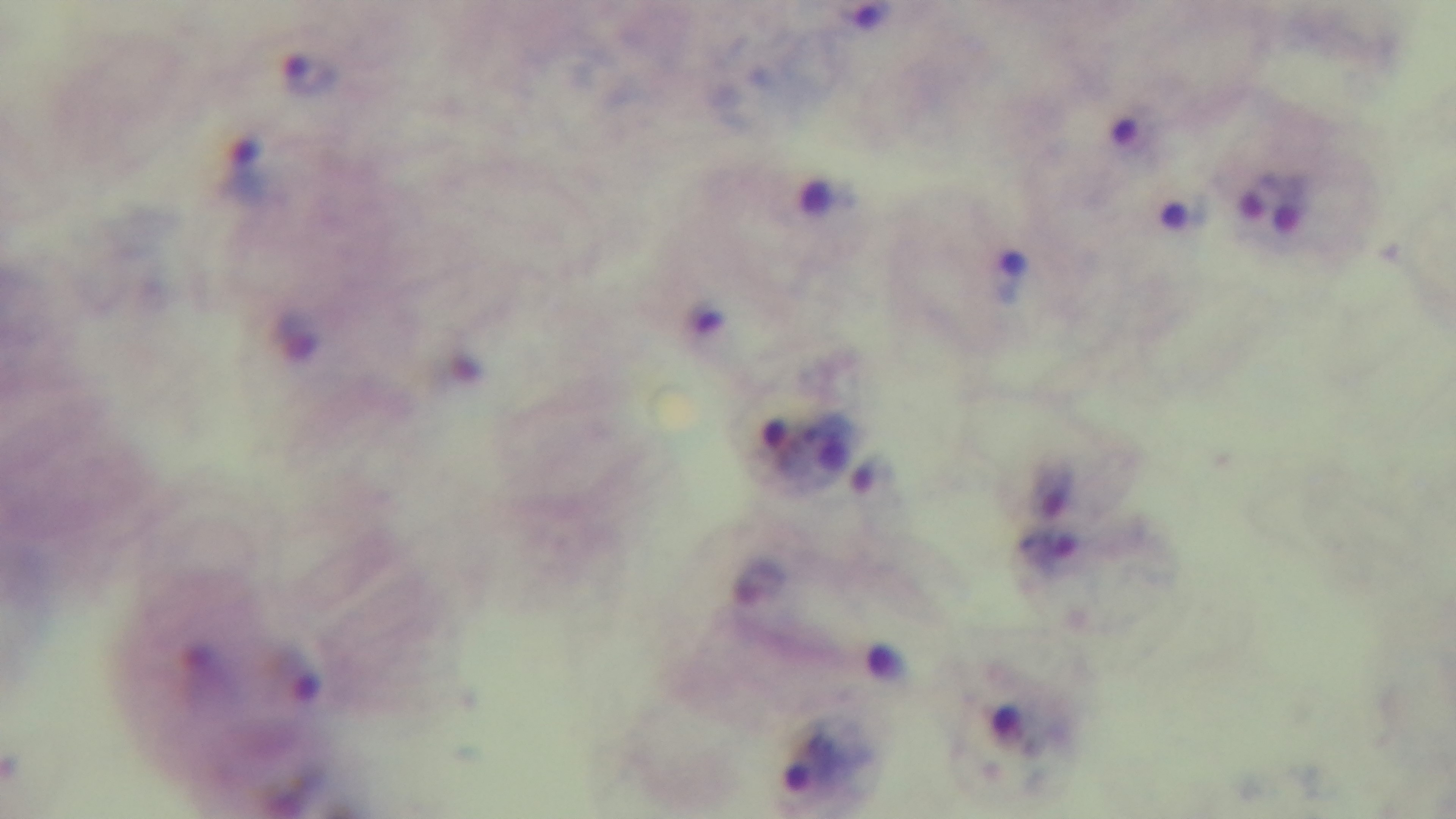

Summary:
  - Preparation: thick
  - Modality: light microscopy
  - Objective: 100x oil immersion
  - Malaria status: positive
  - Field of view: single
  - Capture: mounted 4K digital camera
  - Stain: Giemsa